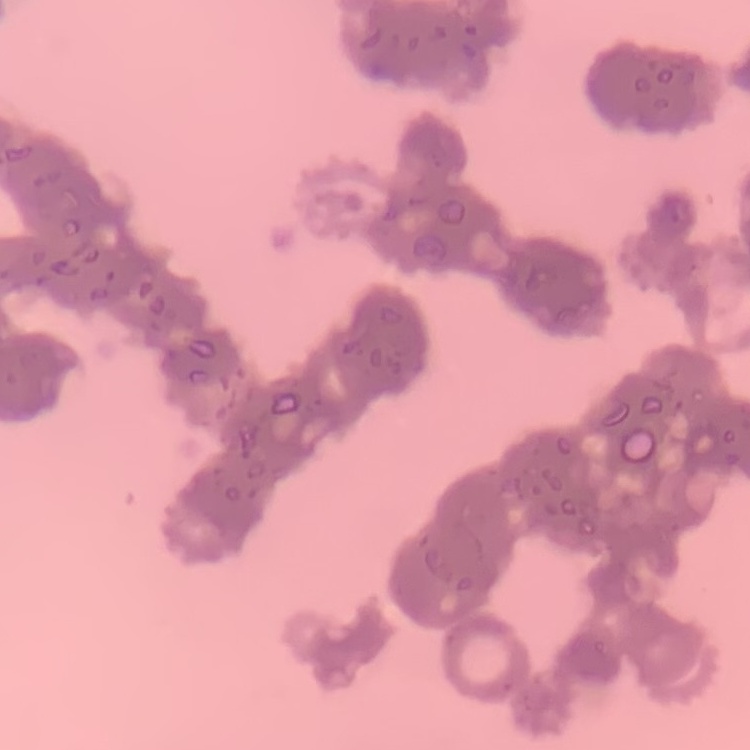
Summary:
  - Red blood cell morphology: rouleaux formation
  - Image type: one tile cut from a larger photomicrograph
  - Preparation: thin blood film
  - Stain: Field's or Giemsa